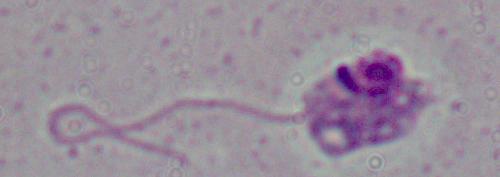
Summary:
  - Modality: micrograph
  - Identification: Leishmania
  - Magnification: 1000x